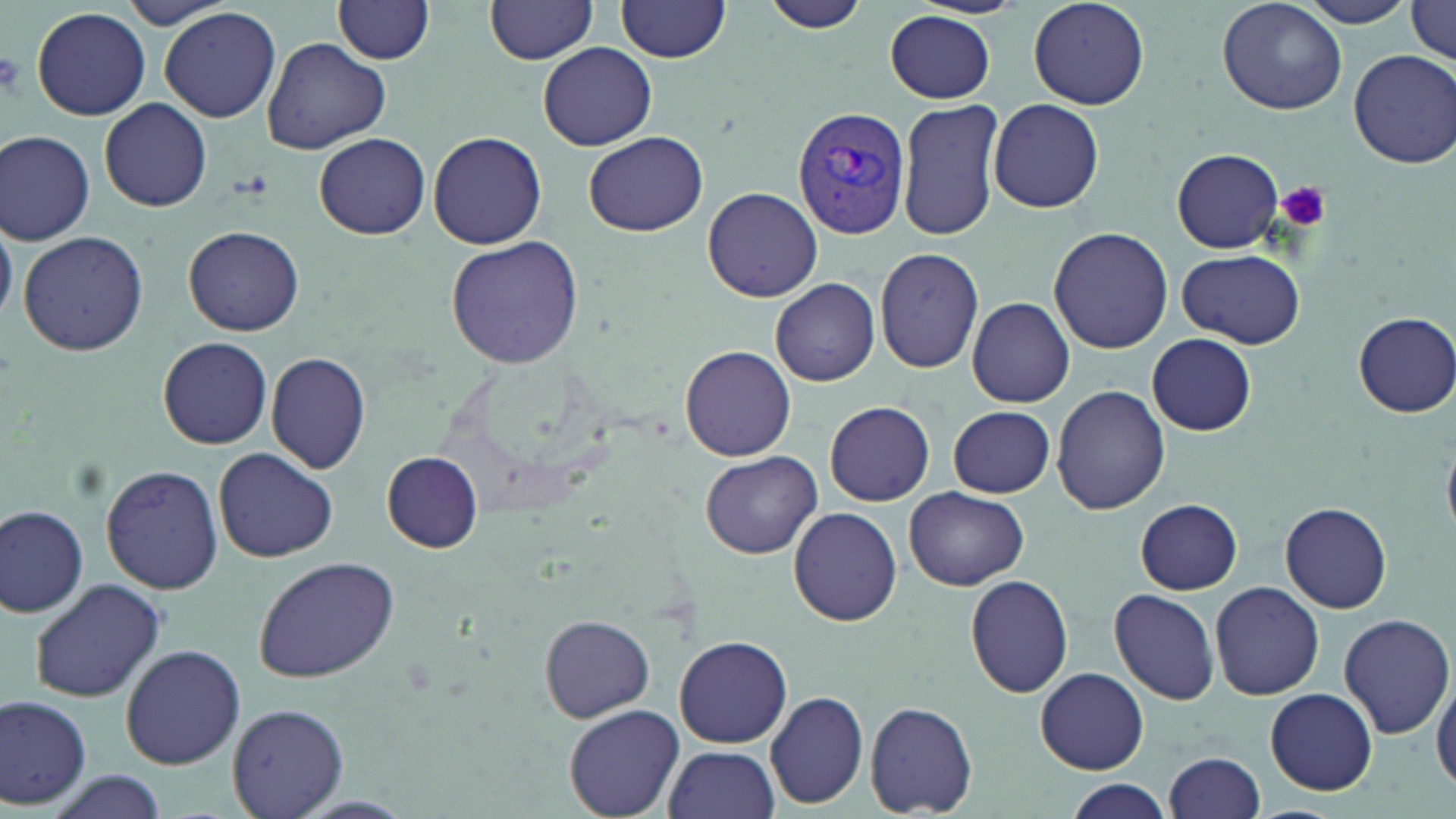 Approximate bounding boxes as (x1, y1, x2, y2) in pixels. Platelet locations: (0, 46, 27, 101), (1272, 179, 1334, 235). Uninfected red blood cell locations: (113, 0, 243, 31), (333, 0, 436, 64), (485, 0, 600, 63), (616, 0, 732, 61), (759, 0, 874, 35), (1027, 0, 1150, 110), (1217, 0, 1347, 116), (1299, 0, 1422, 27), (1407, 1, 1456, 64), (32, 6, 152, 121), (160, 8, 282, 123), (882, 10, 996, 104), (262, 37, 390, 153), (538, 41, 657, 151), (1348, 50, 1456, 169), (897, 98, 1006, 241), (988, 98, 1104, 212), (100, 99, 212, 212), (0, 129, 95, 245), (314, 132, 431, 239), (585, 132, 708, 236), (427, 133, 546, 249), (1172, 148, 1284, 253), (703, 186, 823, 302), (185, 225, 304, 336), (1049, 227, 1175, 355), (18, 230, 149, 356), (446, 236, 583, 369), (874, 246, 986, 373), (1176, 249, 1306, 349), (771, 279, 880, 386), (967, 296, 1075, 407), (1353, 312, 1456, 416), (1147, 333, 1256, 436), (159, 337, 273, 449), (680, 344, 796, 460), (266, 351, 372, 475), (1051, 385, 1172, 514), (824, 401, 935, 507), (948, 405, 1055, 498), (214, 447, 338, 563), (700, 451, 821, 559), (383, 452, 484, 553), (99, 464, 223, 595), (905, 486, 1029, 591), (1135, 499, 1242, 594), (1281, 504, 1392, 612), (1, 505, 90, 617), (788, 507, 902, 627), (252, 555, 400, 683), (965, 573, 1074, 697), (29, 577, 166, 704), (1209, 581, 1324, 699), (1110, 589, 1221, 706), (1339, 613, 1453, 739), (540, 614, 656, 722), (674, 635, 793, 749), (120, 642, 245, 769), (1037, 668, 1148, 774), (1431, 669, 1456, 792), (1265, 688, 1378, 796), (764, 690, 868, 808), (0, 693, 91, 809), (864, 702, 978, 817), (227, 703, 348, 819), (565, 704, 684, 818), (663, 744, 780, 819), (1163, 750, 1267, 819), (40, 771, 167, 819), (1065, 781, 1173, 818). Plasmodium vivax-infected red blood cell locations: (792, 104, 911, 238). Slide-level diagnosis: Plasmodium vivax. Captured at 1000x magnification. Thin blood film. Single field of view. May-Grünwald-Giemsa-stained preparation. Image is 1456×819 pixels. Light microscopy.